Identify the blood parasite species.
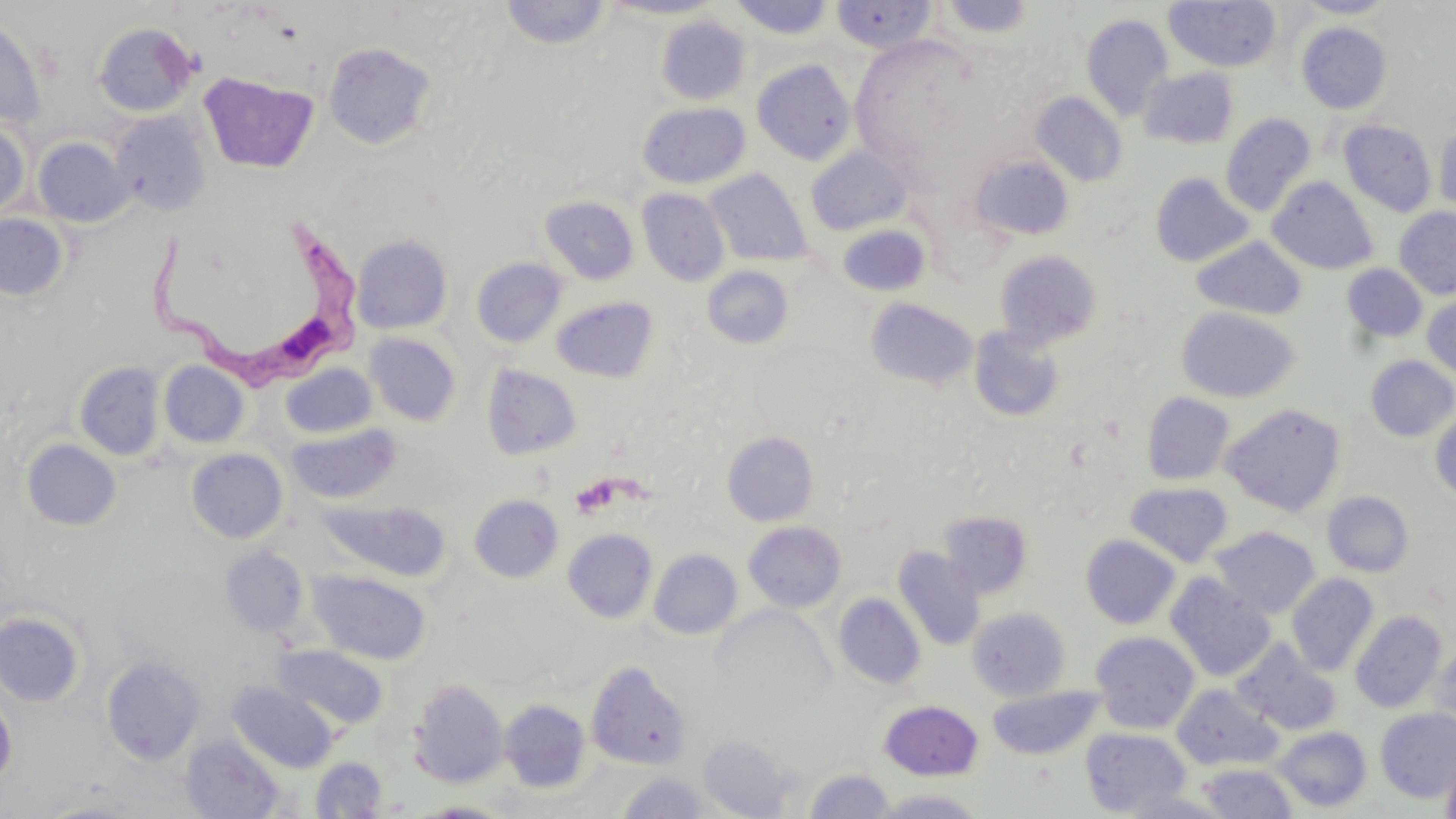

Trypanosoma brucei.

Approximate bounding boxes as (x1, y1, x2, y2) in pixels. Uninfected red blood cell locations: (599, 0, 723, 20), (728, 0, 836, 39), (831, 0, 937, 52), (940, 0, 1036, 38), (1295, 0, 1395, 18), (500, 1, 611, 49), (1164, 1, 1282, 72), (1081, 14, 1173, 120), (656, 16, 750, 105), (0, 19, 47, 129), (93, 22, 199, 116), (1297, 22, 1391, 113), (323, 42, 437, 149), (752, 59, 857, 165), (1139, 67, 1238, 149), (199, 72, 318, 174), (1032, 92, 1127, 186), (638, 102, 750, 188), (111, 110, 212, 217), (1221, 113, 1316, 216), (0, 120, 30, 218), (1340, 120, 1436, 216), (1434, 121, 1456, 215), (34, 137, 133, 226), (807, 146, 912, 235), (971, 156, 1073, 241), (706, 169, 811, 266), (1151, 172, 1252, 267), (1269, 176, 1378, 274), (638, 189, 730, 287), (540, 196, 639, 284), (1394, 207, 1456, 299), (0, 213, 68, 300), (837, 224, 931, 297), (351, 235, 452, 334), (1192, 237, 1306, 319), (995, 250, 1101, 348), (471, 258, 567, 348), (1342, 263, 1428, 342), (702, 266, 794, 349), (1423, 295, 1456, 379), (552, 297, 658, 382), (865, 297, 978, 391), (1177, 307, 1300, 403), (969, 326, 1065, 422), (364, 333, 460, 426), (1366, 356, 1456, 441), (74, 361, 164, 460), (159, 361, 249, 447), (281, 363, 378, 439), (482, 365, 581, 459), (1142, 392, 1235, 485), (1221, 403, 1346, 516), (1430, 410, 1456, 502), (288, 423, 402, 504), (723, 431, 818, 526), (22, 439, 121, 530), (186, 449, 288, 543), (1126, 482, 1233, 567), (1323, 491, 1414, 577), (469, 494, 563, 583), (320, 500, 450, 581), (939, 512, 1032, 598), (744, 521, 846, 612), (1210, 526, 1320, 619), (563, 529, 658, 623), (1082, 534, 1180, 629), (221, 546, 309, 637), (894, 547, 985, 651), (649, 549, 742, 639), (310, 570, 430, 663), (1165, 573, 1276, 681), (1286, 573, 1379, 676), (834, 593, 925, 688), (968, 607, 1070, 701), (1350, 610, 1447, 713), (0, 612, 84, 706), (1090, 631, 1199, 733), (1232, 638, 1342, 735), (1431, 642, 1454, 735), (274, 644, 387, 729), (102, 655, 205, 765), (586, 661, 692, 770), (410, 680, 508, 787), (231, 683, 335, 772), (987, 685, 1104, 760), (1172, 685, 1281, 770), (0, 693, 16, 789), (500, 699, 590, 792), (880, 700, 982, 780), (1375, 708, 1456, 802), (1273, 726, 1372, 811), (1082, 728, 1191, 816), (180, 735, 283, 818), (699, 736, 792, 817), (1441, 741, 1456, 819), (311, 757, 386, 817), (1198, 763, 1297, 818), (805, 769, 895, 818), (617, 772, 713, 817), (872, 789, 987, 818), (37, 796, 146, 818), (415, 801, 513, 817). Trypanosoma brucei locations: (137, 208, 373, 396). Platelet locations: (571, 477, 618, 518). 1000x magnification. One field of a larger specimen. Thin blood film. May-Grünwald-Giemsa stain. Image is 1456×819 pixels. Light microscopy.